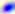
Toxoplasma gondii is shown. Captured at 400x magnification. Micrograph.